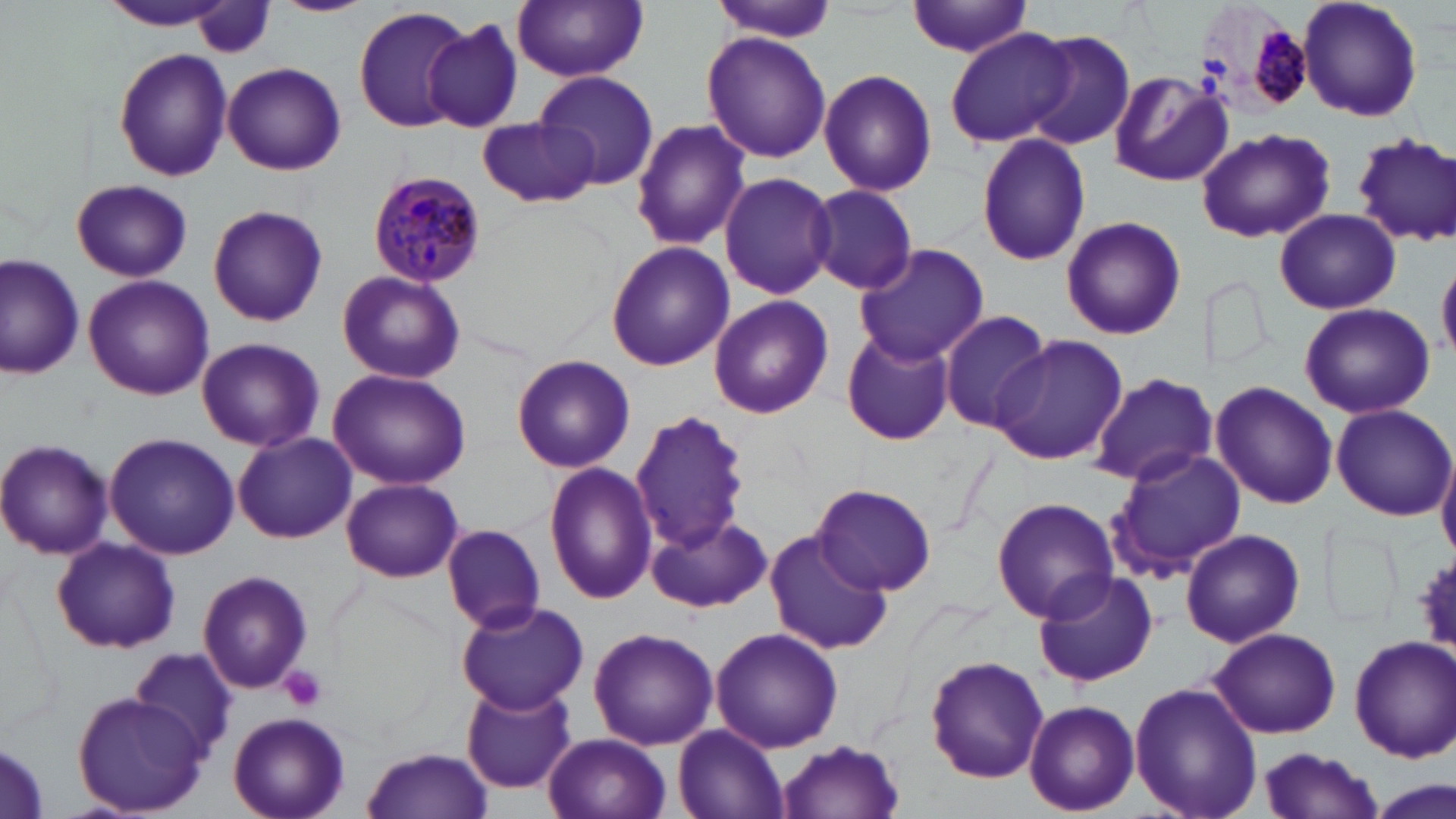
Approximate bounding boxes as (x1,y1)-(x2,y2) corner pairs in pixels. Platelet locations: (279,665)-(328,711). Uninfected red blood cell locations: (95,0)-(240,31), (270,0)-(375,17), (711,0)-(842,41), (1296,0)-(1423,122), (511,1)-(649,80), (907,1)-(1033,58), (194,3)-(274,59), (353,6)-(472,132), (421,19)-(527,134), (943,27)-(1079,147), (702,31)-(832,162), (1022,31)-(1135,152), (114,48)-(231,181), (223,63)-(346,176), (818,68)-(939,196), (534,69)-(659,188), (1107,71)-(1233,188), (478,117)-(599,208), (629,117)-(752,252), (1196,129)-(1334,245), (974,132)-(1092,268), (1353,134)-(1456,247), (718,172)-(839,300), (71,180)-(191,281), (806,184)-(919,295), (207,206)-(328,326), (1274,207)-(1400,313), (1059,214)-(1186,340), (605,241)-(734,372), (852,244)-(990,367), (2,251)-(86,381), (1437,256)-(1456,362), (336,269)-(465,385), (84,275)-(214,401), (707,295)-(834,420), (1299,303)-(1435,420), (938,310)-(1054,432), (841,330)-(957,447), (991,336)-(1128,467), (196,337)-(324,454), (513,353)-(635,473), (327,369)-(472,491), (1089,372)-(1215,487), (1211,382)-(1338,509), (1331,403)-(1456,520), (629,408)-(753,556), (233,431)-(358,545), (105,432)-(239,559), (0,438)-(115,560), (1106,448)-(1247,579), (1438,449)-(1456,560), (544,462)-(659,603), (341,477)-(463,582), (814,484)-(937,596), (992,497)-(1119,625), (647,512)-(772,616), (442,524)-(546,633), (764,528)-(892,657), (1179,529)-(1305,648), (50,538)-(181,654), (1415,552)-(1456,656), (196,570)-(314,693), (1031,571)-(1159,689), (453,599)-(588,716), (589,627)-(719,752), (710,627)-(844,754), (1209,627)-(1342,739), (1348,635)-(1456,760), (128,645)-(242,757), (924,656)-(1050,784), (1129,679)-(1263,819), (462,682)-(578,794), (71,689)-(208,814), (1024,700)-(1139,815), (227,712)-(350,819), (673,723)-(790,819), (544,732)-(670,819), (0,738)-(50,818), (778,739)-(906,819), (361,748)-(493,819), (1254,749)-(1385,818), (1365,775)-(1455,819). Plasmodium malariae-infected red blood cell locations: (1197,2)-(1318,116), (369,169)-(487,289). Slide-level diagnosis: Plasmodium malariae. Image is 1456×819 pixels. 1000x magnification. May-Grünwald-Giemsa stain. Single field of view. Thin blood film. Light microscopy.